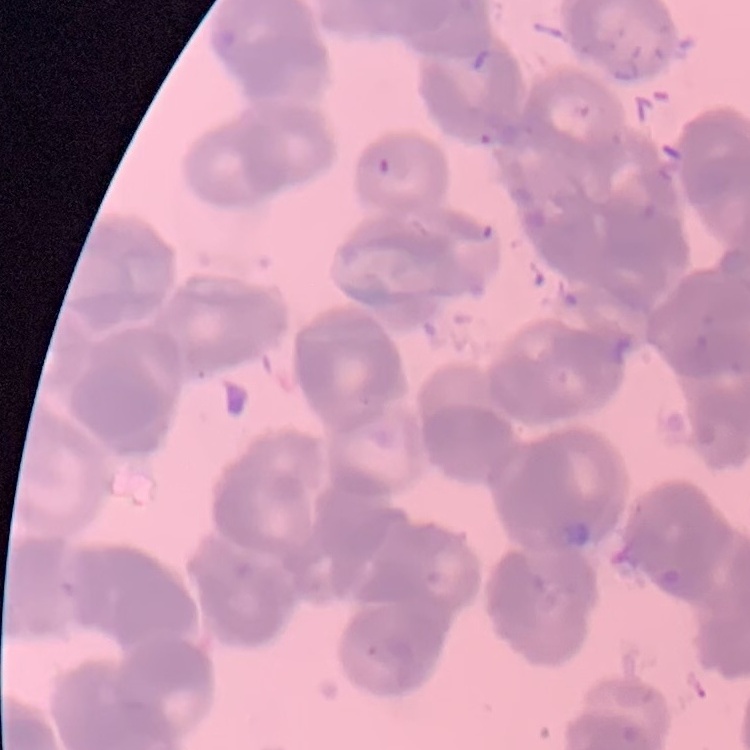
red_blood_cell_morphology: rouleaux formation
stain: Field's or Giemsa
image_type: one tile cut from a larger photomicrograph
preparation: thin blood smear